Assess this cell for malaria.
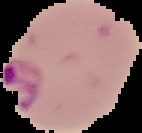

Parasitized.

preparation = thin blood film
image type = segmented cell region on a black background
image size = 142×133 pixels